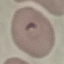

result = malaria parasites detected
image type = automatically extracted cell patch, resized to 64 × 64 pixels
preparation = thin blood smear
stain = Giemsa
capture = smartphone camera at the microscope eyepiece